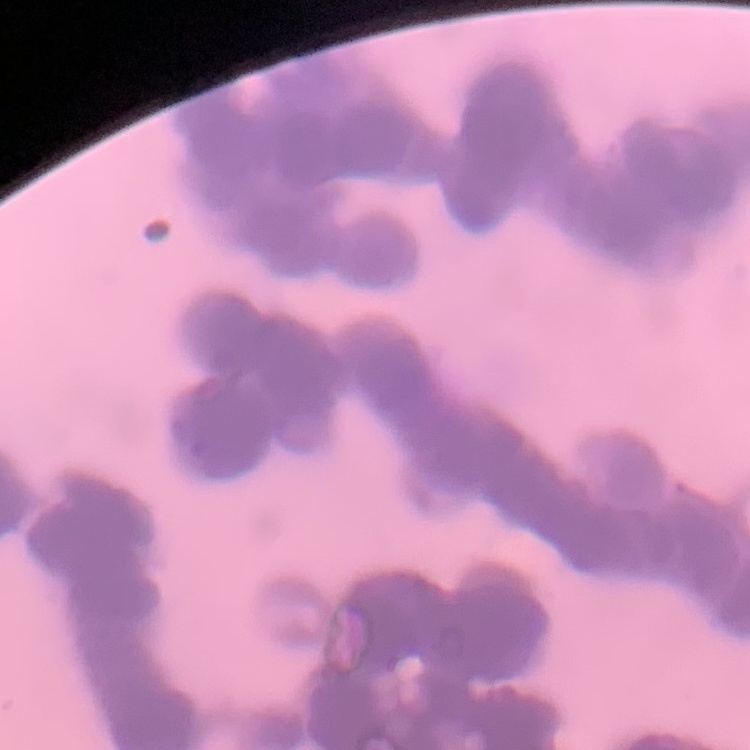
Summary:
  - Erythrocyte morphology: rouleaux formation
  - Image type: square crop of a larger photomicrograph
  - Preparation: thin peripheral smear
  - Stain: Field's or Giemsa